Classify this cell by malaria status.
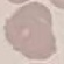
Uninfected.

Summary:
  - Capture: smartphone camera at the microscope eyepiece
  - Image type: cell patch, automatically extracted from a larger field of view and resized to 64 × 64 pixels
  - Preparation: thin blood film
  - Stain: Giemsa